Evaluate for malaria.
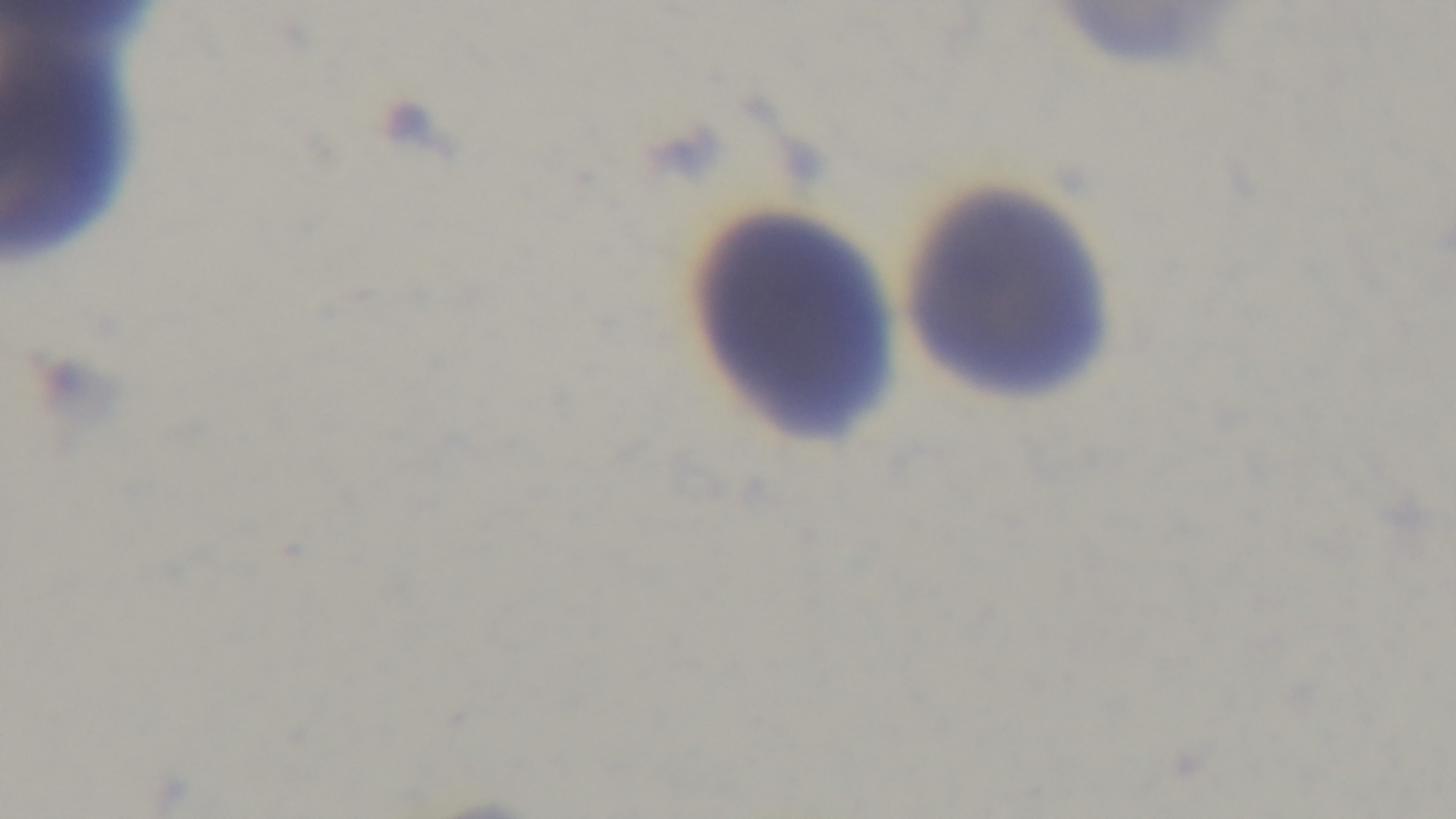

Negative.

Summary:
  - Capture: mounted 4K digital camera
  - Modality: light microscopy
  - Field of view: single
  - Objective: 100x oil immersion
  - Stain: Giemsa
  - Preparation: thin blood film